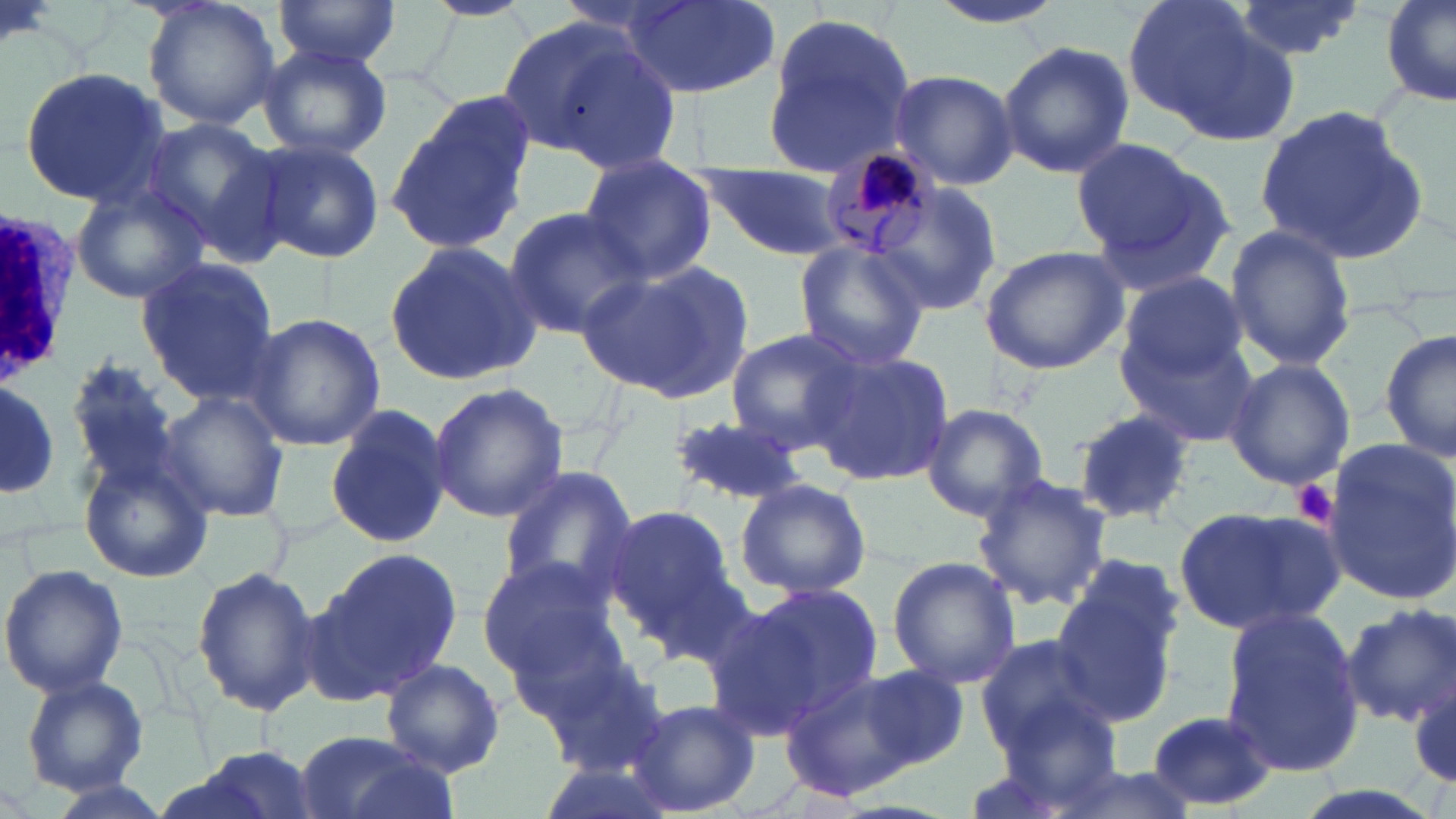

Approximate bounding boxes as (x1,y1)-(x2,y2) corner pairs in pixels. Plasmodium malariae-infected red blood cell locations: (822,142)-(942,259). Platelet locations: (1292,478)-(1339,530). White blood cell locations: (0,202)-(81,386). Uninfected red blood cell locations: (142,0)-(280,132), (272,0)-(404,68), (425,0)-(531,20), (617,0)-(777,98), (925,0)-(1068,31), (1123,0)-(1284,139), (1230,0)-(1369,61), (1380,0)-(1456,110), (760,9)-(920,175), (505,18)-(674,168), (997,40)-(1133,178), (257,44)-(392,161), (20,67)-(169,207), (887,68)-(1019,191), (386,96)-(533,259), (1250,103)-(1431,268), (138,116)-(279,249), (252,137)-(385,265), (1072,139)-(1239,293), (576,156)-(717,285), (695,162)-(847,259), (858,171)-(1005,322), (68,181)-(208,306), (502,206)-(647,339), (1224,225)-(1356,369), (383,241)-(544,386), (794,241)-(931,372), (977,244)-(1131,375), (135,258)-(280,397), (579,258)-(754,402), (1117,270)-(1249,387), (244,311)-(386,451), (1118,326)-(1260,445), (724,327)-(865,451), (1381,328)-(1456,466), (805,348)-(955,489), (64,351)-(192,501), (1223,357)-(1355,489), (0,381)-(60,495), (428,381)-(570,524), (156,391)-(290,521), (325,403)-(452,551), (921,403)-(1051,522), (1070,410)-(1199,528), (665,414)-(808,506), (1319,439)-(1456,604), (77,455)-(211,581), (495,463)-(639,606), (971,475)-(1114,611), (734,477)-(872,600), (1174,503)-(1344,636), (604,507)-(738,643), (312,545)-(466,702), (475,554)-(622,681), (886,556)-(1021,687), (0,564)-(128,699), (193,565)-(321,715), (1052,577)-(1181,728), (740,581)-(883,725), (693,600)-(839,739), (1344,603)-(1456,727), (1220,609)-(1365,775), (973,633)-(1114,756), (532,651)-(674,780), (379,658)-(507,777), (776,663)-(943,801), (851,663)-(970,772), (1410,675)-(1455,792), (20,676)-(149,797), (624,697)-(762,818), (980,706)-(1129,819), (1143,710)-(1282,808), (293,729)-(455,819), (174,746)-(326,819). Slide-level diagnosis: Plasmodium malariae. Light microscopy. Image is 1456×819 pixels. Thin blood smear. One field of a larger specimen. May-Grünwald-Giemsa-stained preparation. 1000x magnification.